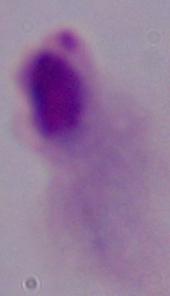 Photomicrograph. Captured at 1000x magnification. A trichomonad is shown.